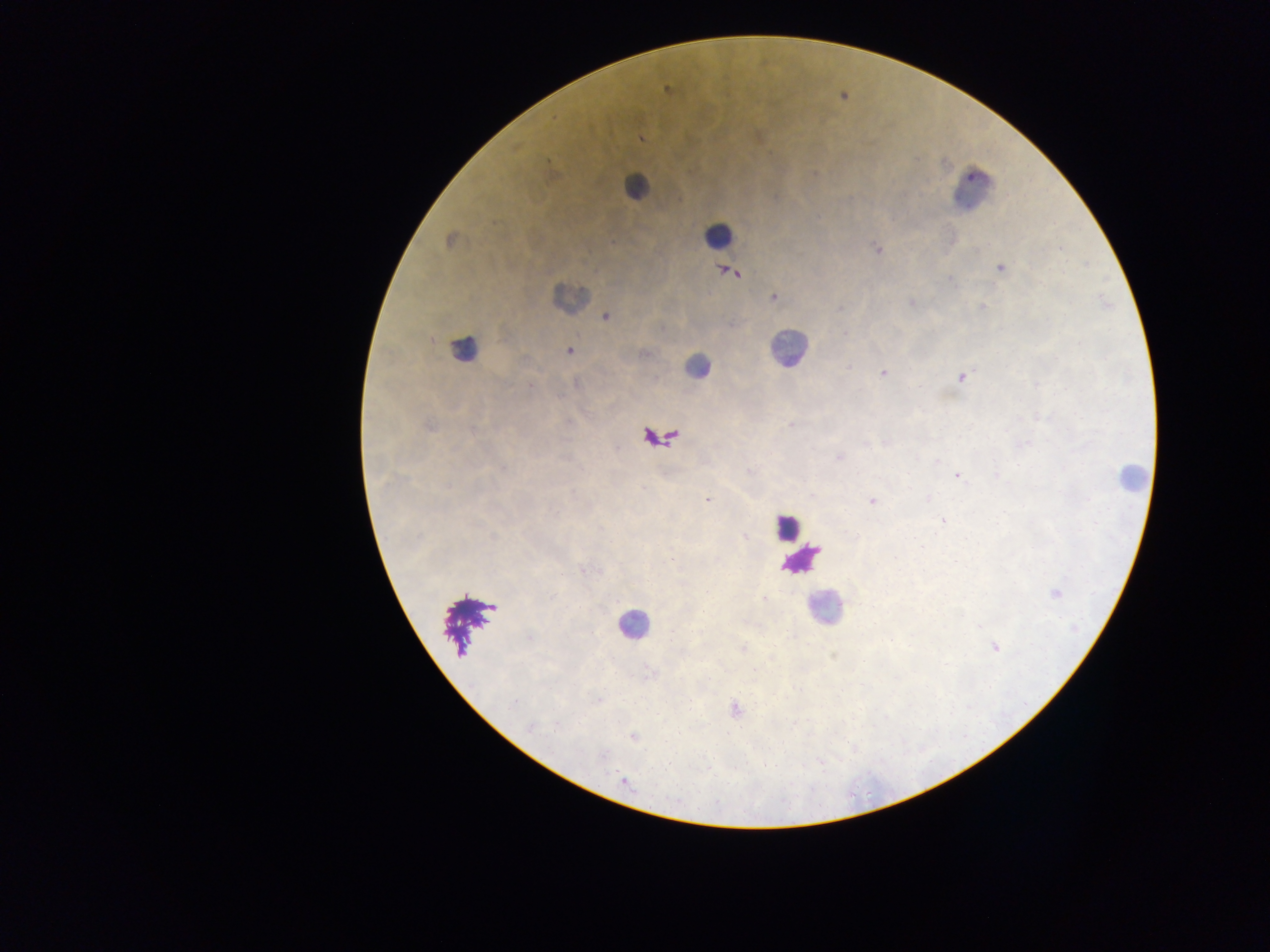

Approximate centers as (x, y) in pixels.
Summary:
  - Malaria parasite locations: (667, 89), (641, 138), (814, 174), (449, 241), (877, 248), (1059, 248), (1000, 268), (732, 272), (949, 279), (774, 297), (911, 302), (981, 306), (839, 308), (605, 317), (844, 334), (569, 351), (645, 354), (849, 366), (883, 374), (962, 377), (530, 386), (790, 425), (430, 427), (865, 444), (838, 457), (937, 460), (996, 475), (957, 476), (927, 498), (707, 499), (872, 501), (942, 520), (744, 536), (1055, 594), (764, 599), (530, 638), (995, 646), (743, 648), (598, 700), (514, 703), (734, 708), (556, 727), (530, 728), (634, 738), (623, 781)
  - Leukocyte locations: (634, 186), (973, 190), (718, 234), (569, 297), (463, 347), (788, 348), (697, 366), (1131, 476), (787, 527), (824, 607), (633, 625)
  - Preparation: thick blood smear
  - Image size: 1270×952 pixels
  - Field of view: single
  - Country: Ghana
  - Capture: mobile-phone photograph through a microscope